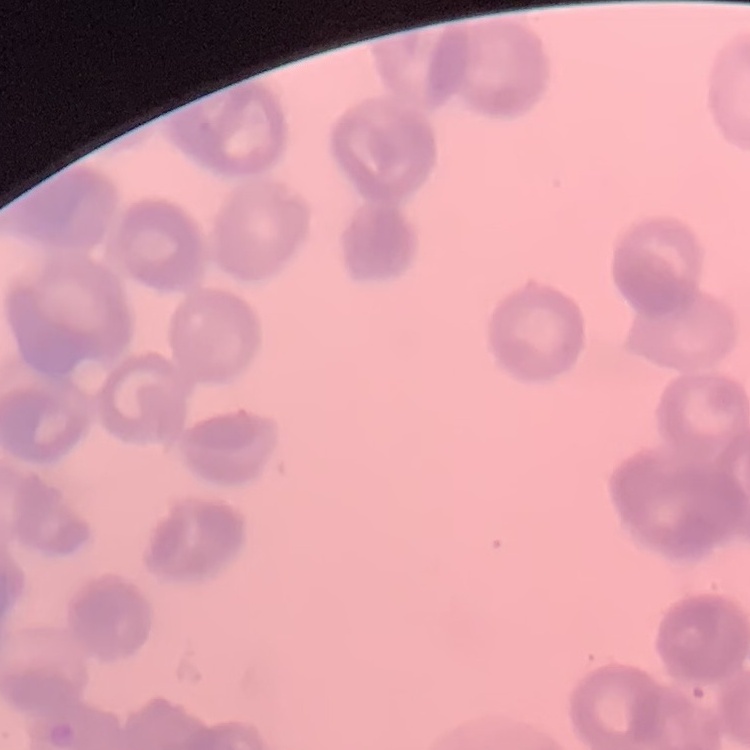

The red blood cells exhibit rouleaux formation. Stained with either Field's or Giemsa. Thin blood film. One tile cut from a larger photomicrograph.